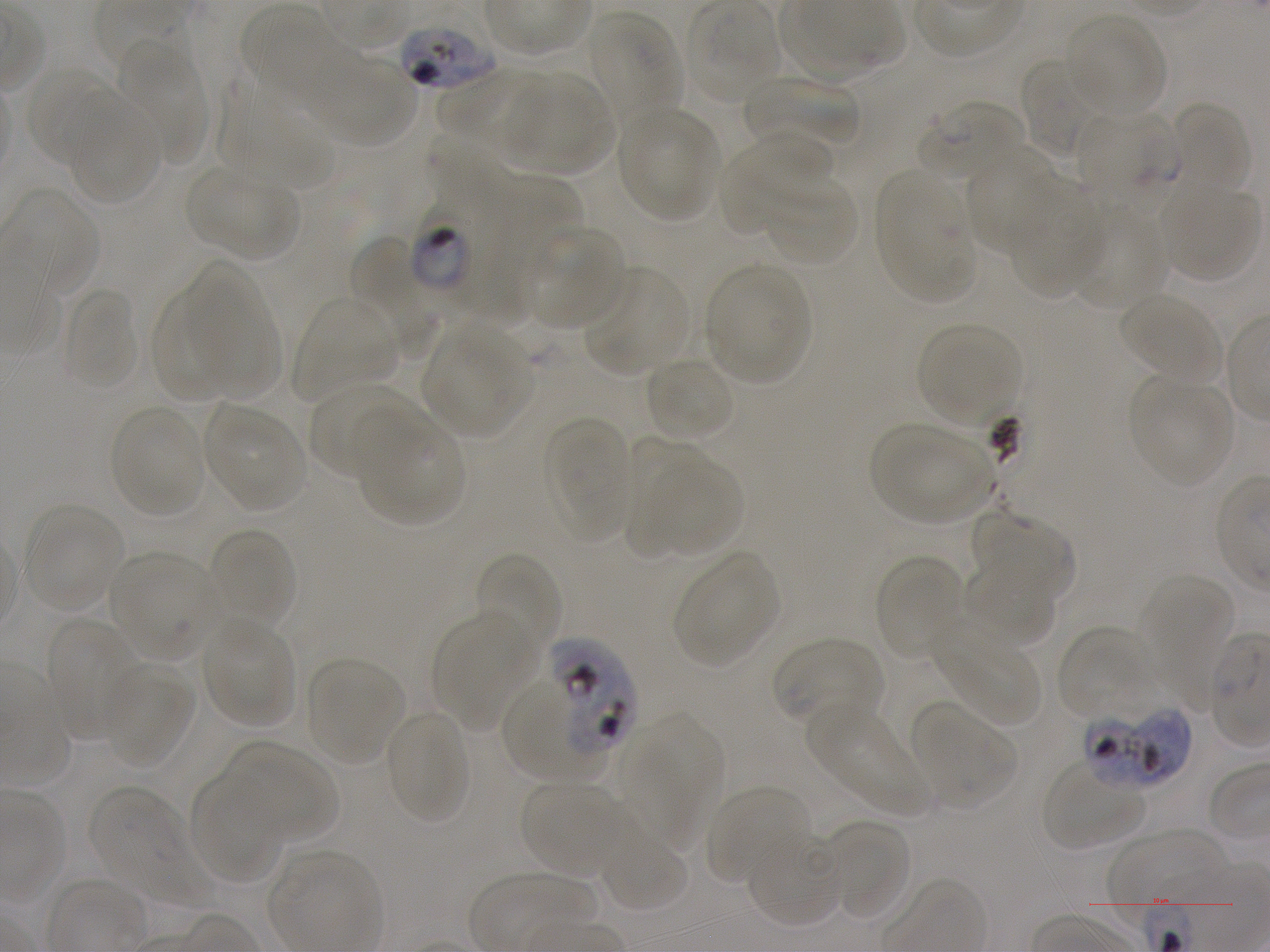 Approximate bounding boxes as {x1, y1, x2, y2} in pixels. Not every red blood cell is marked. A life-cycle stage — or a range of stages, where the recorded stages span more than one — follows each staged infected red blood cell. Locations of infected red blood cells: {413, 182, 505, 295} trophozoite; {548, 639, 637, 761}; {1088, 706, 1192, 790}. Locations of red blood cells of indeterminate infection status: {397, 23, 496, 92}, {918, 99, 1023, 181}, {504, 680, 595, 784}. Locations of uninfected red blood cells: {686, 1, 778, 102}, {241, 5, 346, 101}, {583, 13, 680, 136}, {1066, 15, 1165, 116}, {123, 45, 208, 166}, {308, 52, 418, 145}, {1019, 57, 1106, 159}, {26, 67, 117, 166}, {437, 68, 549, 149}, {505, 72, 613, 175}, {741, 75, 860, 147}, {216, 79, 333, 188}, {66, 95, 161, 205}, {1168, 102, 1251, 196}, {618, 105, 719, 219}, {1078, 109, 1178, 212}, {720, 136, 834, 233}, {965, 149, 1054, 255}, {186, 166, 293, 256}, {875, 170, 974, 301}, {478, 173, 580, 301}, {761, 177, 858, 267}, {1008, 181, 1103, 298}, {1161, 183, 1259, 281}, {1071, 203, 1166, 312}, {526, 227, 628, 330}, {353, 236, 438, 361}, {704, 263, 809, 385}, {583, 266, 690, 376}, {187, 269, 278, 393}, {61, 288, 139, 391}, {151, 289, 232, 404}, {1118, 294, 1222, 385}, {292, 297, 398, 400}, {916, 321, 1021, 427}, {424, 325, 527, 436}, {644, 356, 735, 440}, {1129, 377, 1232, 486}, {310, 382, 416, 478}, {203, 402, 309, 511}, {108, 403, 207, 518}, {356, 416, 465, 525}, {545, 416, 630, 541}, {870, 424, 995, 523}, {623, 433, 701, 554}, {647, 458, 742, 556}, {23, 505, 124, 609}, {972, 513, 1075, 604}, {207, 527, 297, 626}, {108, 551, 221, 659}, {674, 551, 778, 667}, {473, 553, 560, 658}, {873, 553, 966, 660}, {964, 559, 1055, 646}, {1143, 578, 1237, 713}, {432, 611, 538, 729}, {200, 617, 296, 727}, {47, 620, 140, 741}, {934, 624, 1038, 726}, {1056, 626, 1156, 719}, {772, 637, 885, 726}, {305, 657, 405, 766}, {102, 665, 194, 767}, {913, 702, 1015, 807}, {807, 706, 929, 814}, {385, 709, 469, 823}, {629, 717, 717, 849}, {224, 741, 337, 843}, {1042, 761, 1145, 849}, {188, 773, 285, 885}, {520, 781, 627, 876}, {706, 784, 810, 885}, {88, 788, 222, 911}, {820, 819, 910, 919}, {1107, 829, 1233, 927}, {745, 830, 842, 930}, {598, 833, 690, 913}. Image is 1270×952 pixels. Blood group of the donor: A+. Thin blood smear. One field from this slide. Giemsa stain. 100x objective under oil immersion, numerical aperture 1.25. Plasmodium falciparum strain NF54 maintained in static in-vitro culture.